Give the preparation type.
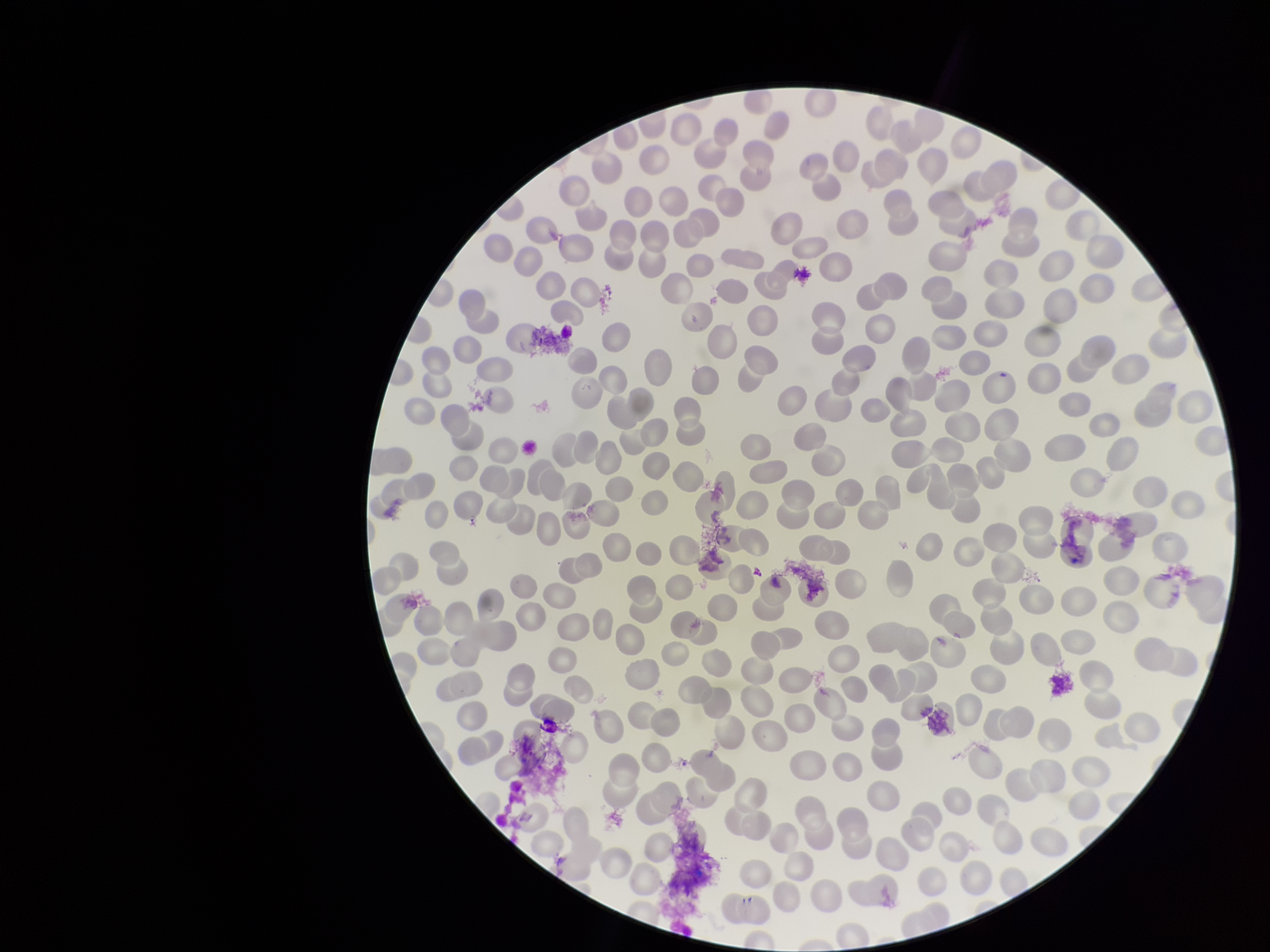
Thin.

Photographed through the microscope eyepiece with a smartphone camera. Image is 1270×952 pixels. Patient malaria status: negative. Single field of view. Giemsa stain. Parasitized red blood cell count: 0. Red blood cell count: 269. Parasitized red blood cells: none seen.